Locate malaria parasites and leukocytes.
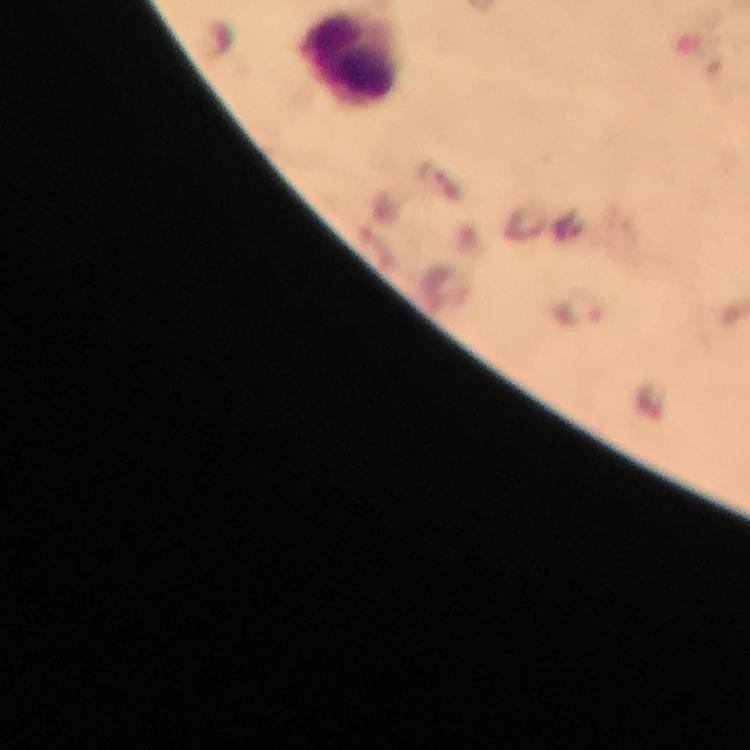

Approximate centers as {x, y} in pixels.
Malaria parasites: {580, 309}.
Leukocytes: {351, 62}.

image size = 750×750 pixels
immersion oil = applied
magnification = 100x
cropped from = a single field of view
context = from a malaria diagnostic workup
preparation = thick blood smear
capture = smartphone mounted on the microscope
stain = Giemsa